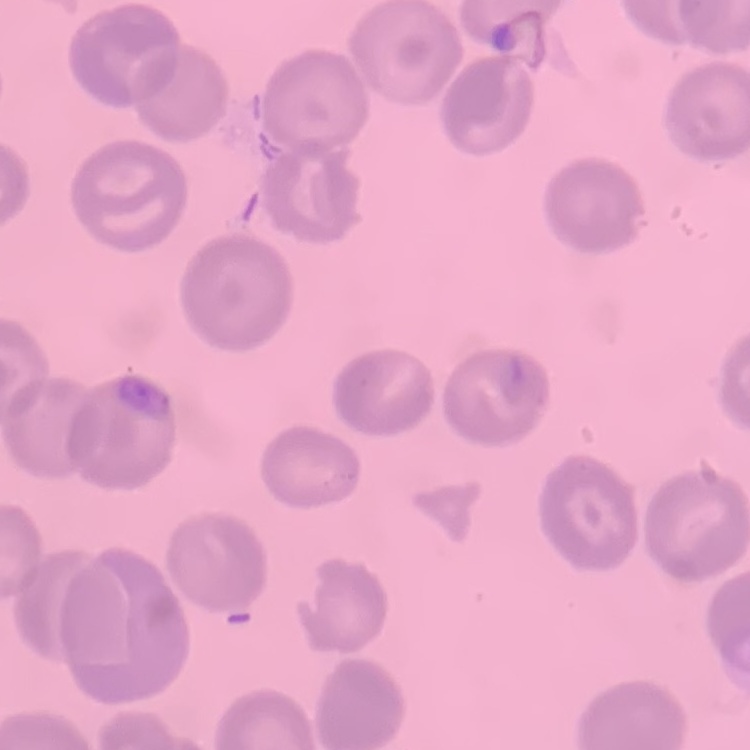
Summary:
  - Erythrocyte morphology: no rouleaux formation
  - Stain: Field's or Giemsa
  - Preparation: thin blood film
  - Image type: one tile cut from a larger photomicrograph